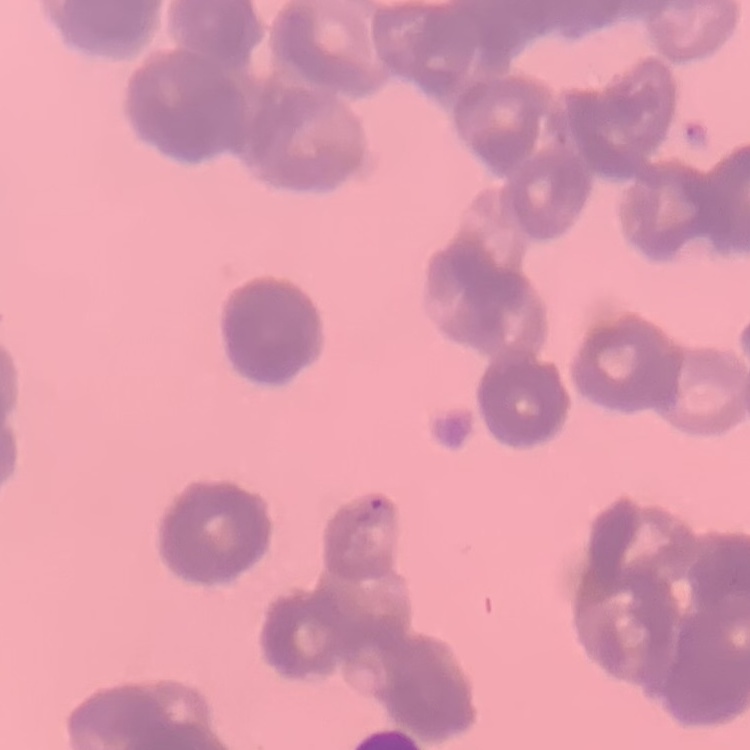

The red blood cells show rouleaux formation. Square crop of a larger photomicrograph. Stained with either Field's or Giemsa. Thin blood film.